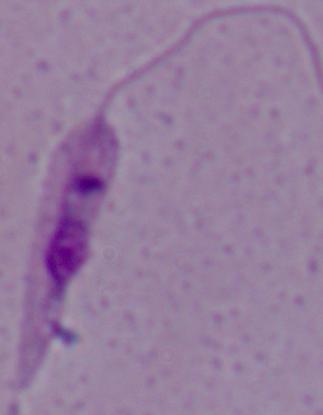

magnification = 1000x
modality = micrograph
identification = Leishmania